Identify the preparation type.
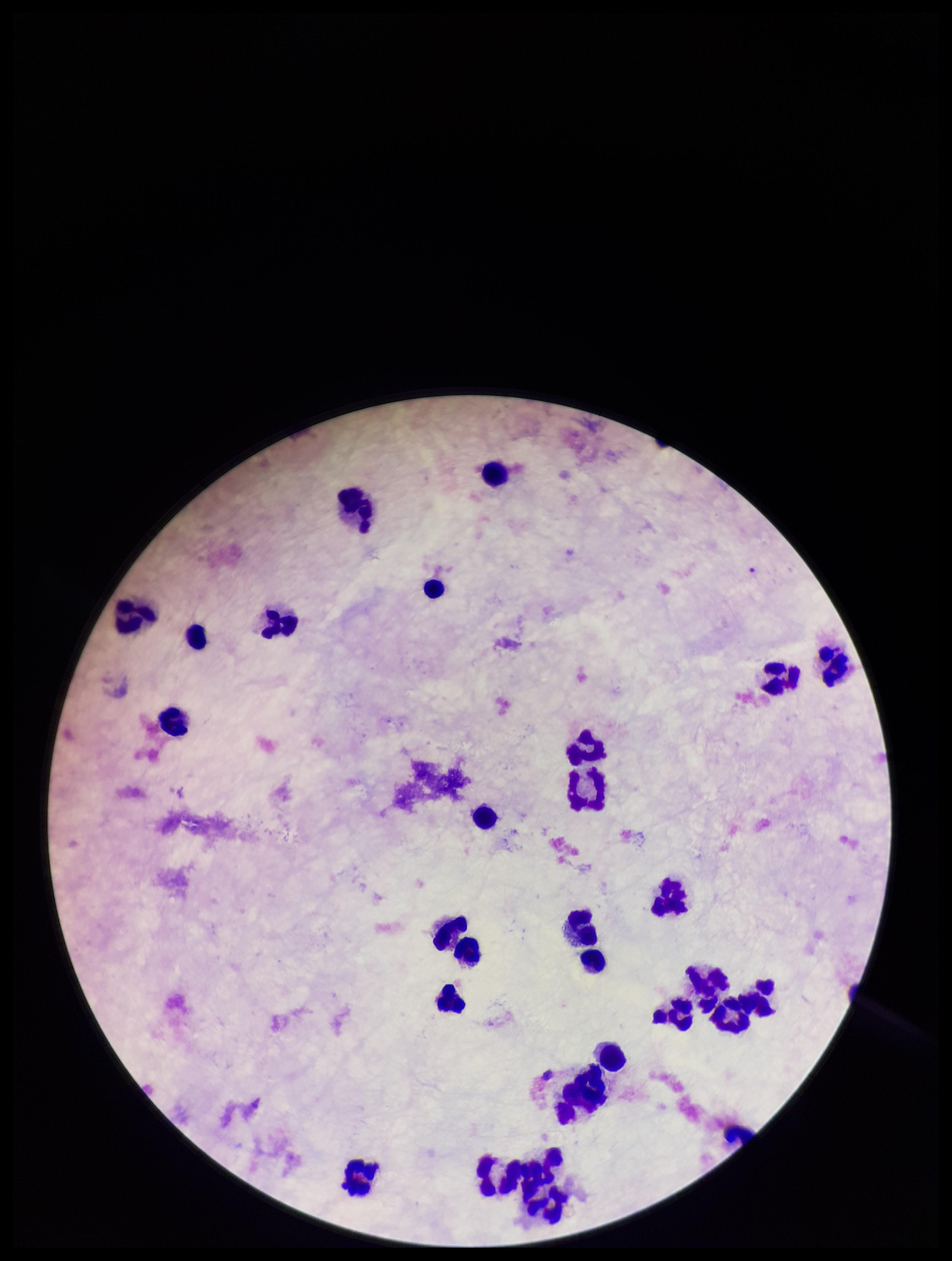
Thick.

plasmodium_parasites: none detected
stain: Giemsa
capture: smartphone photograph through the microscope eyepiece
patient_malaria_status: negative
leukocyte_count: 28
field_of_view: single
image_size: 952×1261 pixels
parasite_count: 0